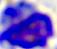

Micrograph. 400x magnification. A leukocyte is seen.